Describe the morphology of the erythrocytes.
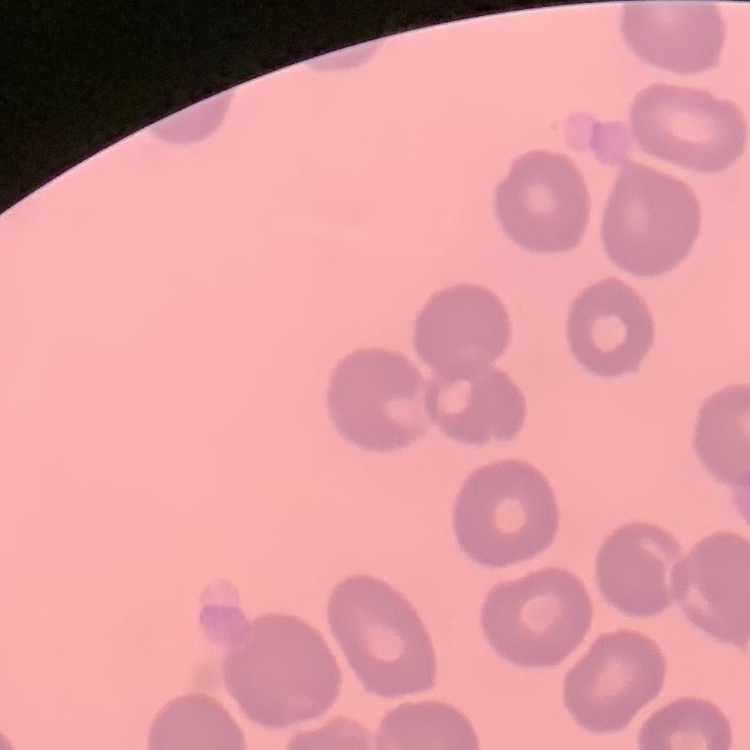

They show no rouleaux formation.

preparation = thin peripheral smear
image type = one tile cut from a larger photomicrograph
stain = Field's or Giemsa